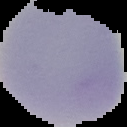
Summary:
  - Image size: 127×127 pixels
  - Image type: cell region segmented out of the field of view; surrounding area masked to black
  - Result: no malaria parasites detected
  - Preparation: thin blood film